Identify the cell.
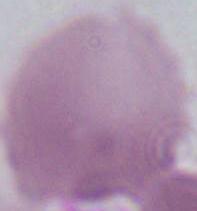
An erythrocyte.

magnification = 1000x
modality = photomicrograph